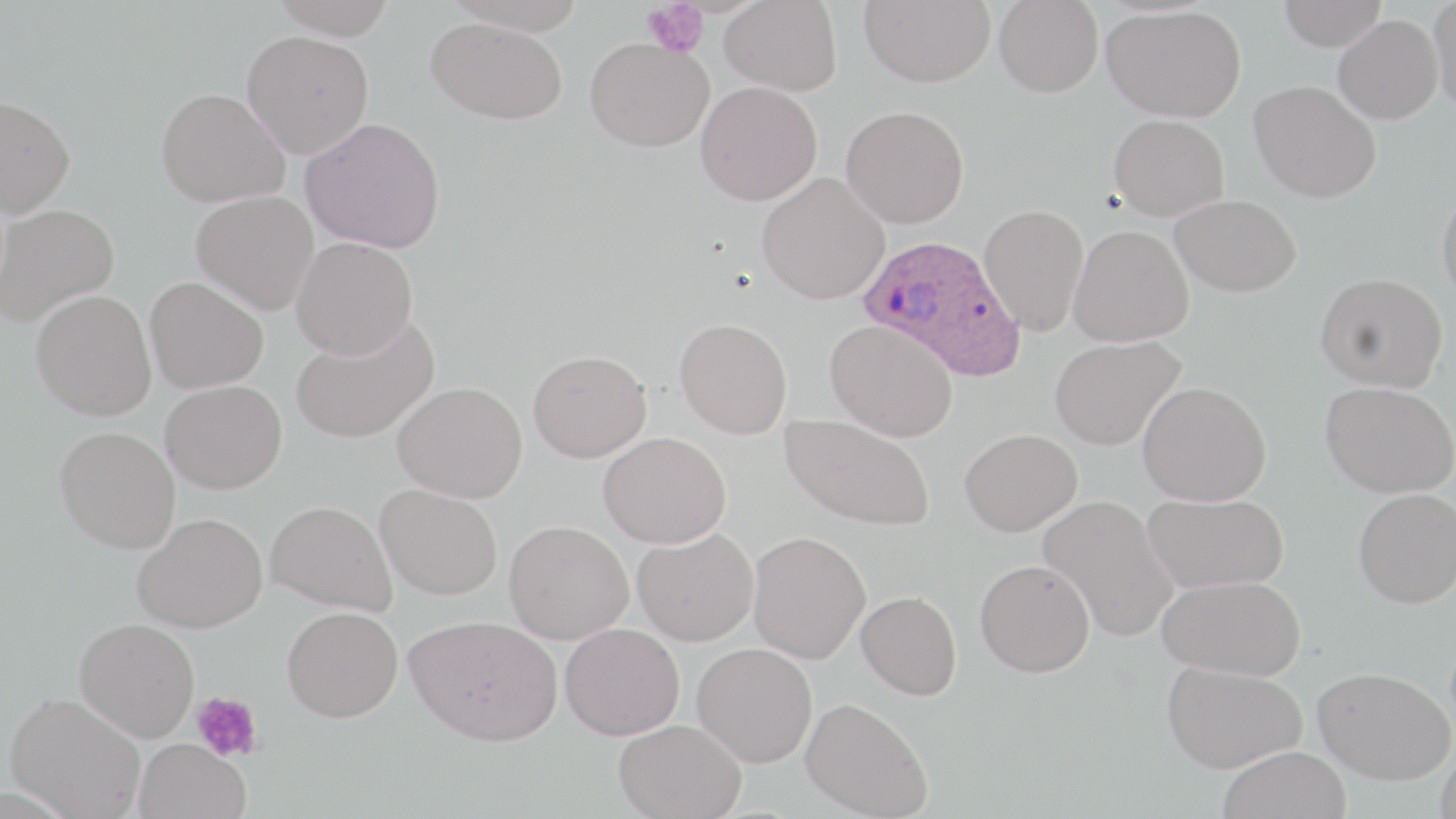

Approximate bounding boxes as (x1, y1, x2, y2) in pixels. Plasmodium ovale-infected red blood cell locations: (856, 233, 1026, 381). Uninfected red blood cell locations: (268, 0, 398, 40), (442, 0, 591, 34), (720, 0, 842, 95), (859, 0, 995, 87), (995, 0, 1103, 97), (1277, 0, 1387, 51), (1428, 0, 1456, 114), (1102, 5, 1246, 122), (1333, 15, 1443, 124), (426, 17, 568, 124), (241, 30, 374, 158), (585, 37, 713, 152), (695, 81, 823, 206), (1248, 81, 1382, 203), (155, 87, 289, 208), (0, 95, 76, 217), (841, 105, 969, 228), (1109, 114, 1229, 221), (301, 117, 446, 254), (757, 172, 890, 304), (1437, 186, 1456, 312), (191, 191, 319, 315), (1169, 194, 1300, 297), (0, 204, 119, 326), (980, 204, 1089, 335), (1068, 224, 1194, 347), (291, 237, 418, 359), (1316, 272, 1448, 392), (145, 276, 269, 392), (31, 290, 157, 421), (290, 315, 440, 444), (674, 317, 793, 439), (825, 320, 958, 441), (1049, 335, 1185, 449), (528, 349, 652, 462), (160, 380, 287, 494), (393, 380, 528, 503), (1137, 381, 1272, 506), (1321, 382, 1456, 498), (779, 414, 935, 531), (55, 426, 180, 553), (959, 428, 1083, 535), (598, 431, 731, 548), (375, 484, 502, 600), (1354, 488, 1456, 608), (1142, 492, 1289, 593), (1038, 495, 1180, 642), (266, 500, 398, 615), (132, 513, 267, 633), (504, 520, 633, 643), (632, 528, 759, 646), (747, 531, 871, 663), (975, 559, 1095, 677), (1158, 575, 1306, 679), (856, 590, 962, 700), (282, 606, 403, 722), (405, 614, 563, 745), (75, 618, 199, 740), (560, 622, 684, 740), (692, 643, 818, 767), (1162, 660, 1307, 772), (1313, 666, 1455, 785), (5, 692, 146, 818), (801, 697, 933, 819), (614, 718, 746, 818), (133, 739, 251, 819), (1435, 744, 1456, 819), (1217, 745, 1352, 819). Platelet locations: (641, 1, 709, 57), (191, 691, 263, 761). Slide-level diagnosis: Plasmodium ovale. May-Grünwald-Giemsa stain. Thin blood smear. One field of a larger specimen. Image is 1456×819 pixels. Captured at 1000x magnification. Optical microscopy.